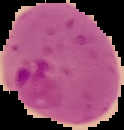 From a thin blood film. The area outside the segmented cell region is set to black. Image is 124×130 pixels. Malaria status: parasitized.